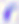

modality = photomicrograph
identification = Toxoplasma gondii
magnification = 400x